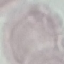

Summary:
  - Result: no malaria parasites detected
  - Capture: smartphone camera at the microscope eyepiece
  - Stain: Giemsa
  - Preparation: thin smear
  - Image type: automatically extracted cell patch, resized to 64 × 64 pixels